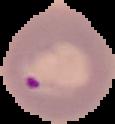

Image is 115×124 pixels. Result: Plasmodium parasites detected. Segmented cell region on a black background. From a thin blood film.